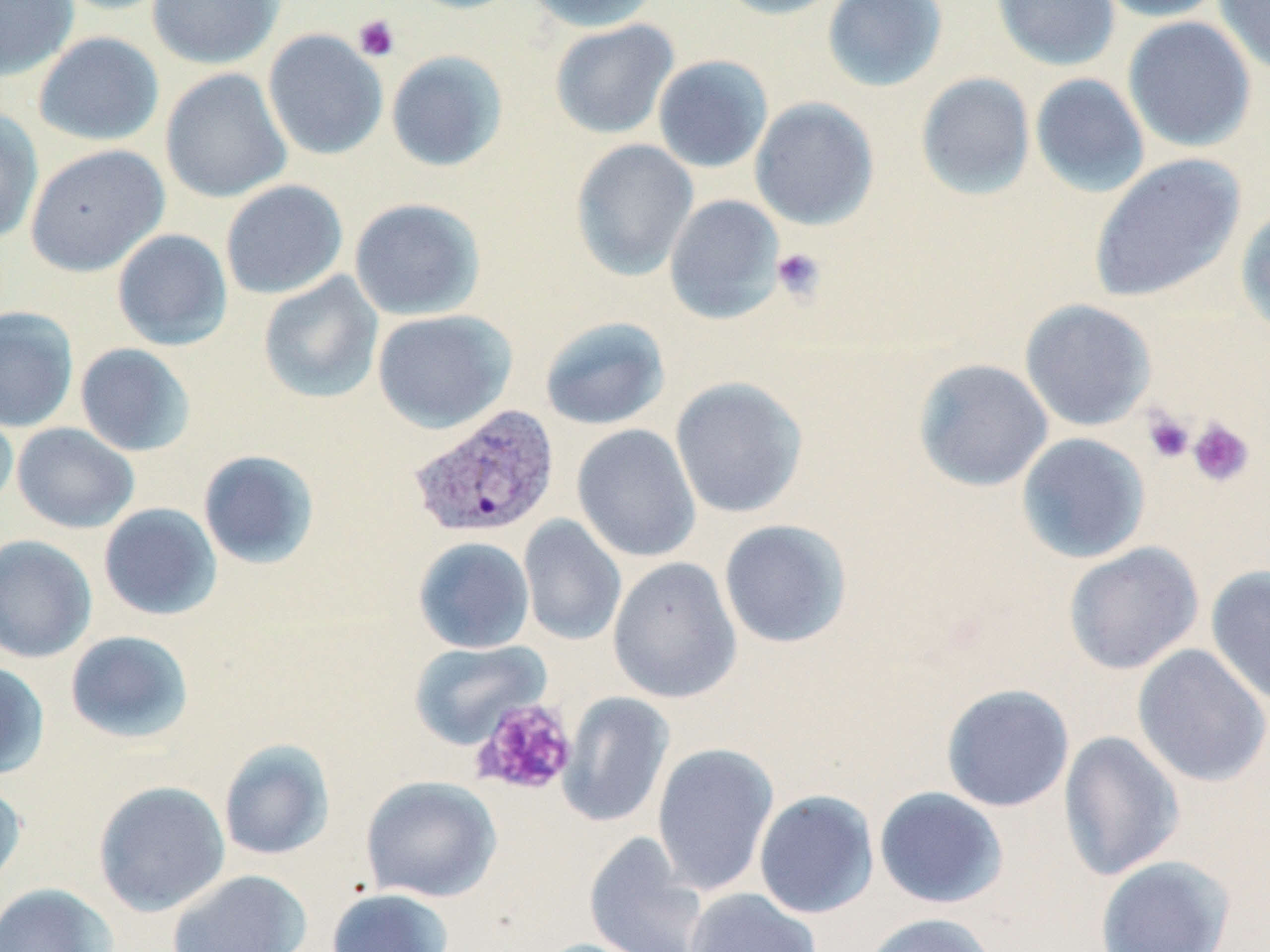

slide_level_diagnosis: Plasmodium vivax
preparation: thin blood smear
modality: optical microscopy
plasmodium_vivax_infected_red_blood_cell_locations: 'approximate bounding boxes as (x1,y1)-(x2,y2) corner pairs in pixels: (408,404)-(560,540)'
field_of_view: one of a larger specimen
magnification: 1000x
uninfected_red_blood_cell_locations: 'approximate bounding boxes as (x1,y1)-(x2,y2) corner pairs in pixels: (0,0)-(78,81), (50,0)-(178,15), (147,0)-(284,69), (402,0)-(526,14), (524,0)-(662,32), (711,0)-(849,20), (822,0)-(948,92), (992,0)-(1121,71), (1093,0)-(1229,22), (1213,0)-(1270,77), (1122,16)-(1257,153), (549,19)-(679,140), (263,29)-(388,160), (33,32)-(164,147), (385,50)-(509,172), (652,55)-(773,173), (160,68)-(292,203), (915,72)-(1035,200), (1030,73)-(1150,198), (750,97)-(880,230), (0,107)-(44,243), (570,139)-(698,281), (25,144)-(170,276), (1088,153)-(1247,304), (220,180)-(348,300), (664,194)-(785,324), (348,197)-(485,320), (1235,205)-(1270,340), (112,228)-(232,351), (257,272)-(384,404), (1019,298)-(1157,431), (0,306)-(79,432), (372,309)-(516,433), (539,316)-(670,430), (75,343)-(196,457), (912,358)-(1053,492), (670,376)-(807,519), (0,401)-(19,513), (12,422)-(139,534), (572,424)-(701,563), (1016,433)-(1150,564), (198,450)-(320,569), (98,503)-(222,621), (518,515)-(627,647), (718,519)-(852,648), (0,535)-(97,664), (413,536)-(535,654), (1063,542)-(1205,675), (608,557)-(742,704), (1204,565)-(1270,707), (64,630)-(195,745), (408,640)-(551,750), (1132,644)-(1270,787), (0,660)-(50,780), (941,684)-(1075,813), (558,692)-(674,828), (1058,730)-(1185,881), (218,739)-(335,861), (652,742)-(779,896), (360,775)-(503,903), (0,779)-(28,893), (93,780)-(230,917), (874,786)-(1008,909), (753,789)-(879,919), (584,832)-(710,952), (1095,855)-(1235,951), (166,870)-(312,952), (0,883)-(117,952), (326,887)-(453,952), (685,887)-(822,952), (860,912)-(999,952), (528,937)-(662,952)'
image_size: 1270×952 pixels
platelet_locations: 'approximate bounding boxes as (x1,y1)-(x2,y2) corner pairs in pixels: (353,14)-(400,61), (771,247)-(826,303), (1142,409)-(1195,463), (1187,417)-(1254,488), (471,698)-(578,797)'
stain: May-Grünwald-Giemsa